State which parasite is depicted.
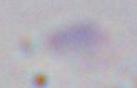
This is Toxoplasma gondii.

1000x magnification. Micrograph.